Classify this cell by malaria status.
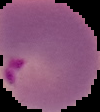

It is parasitized.

image type = segmented cell region with the area outside set to black
preparation = thin blood film
image size = 100×112 pixels